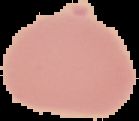
From a thin blood smear. Cell region segmented out of the field of view; the surrounding area is masked to black. Image is 139×121 pixels. Malaria status: uninfected.